Outline each uninfected red blood cell.
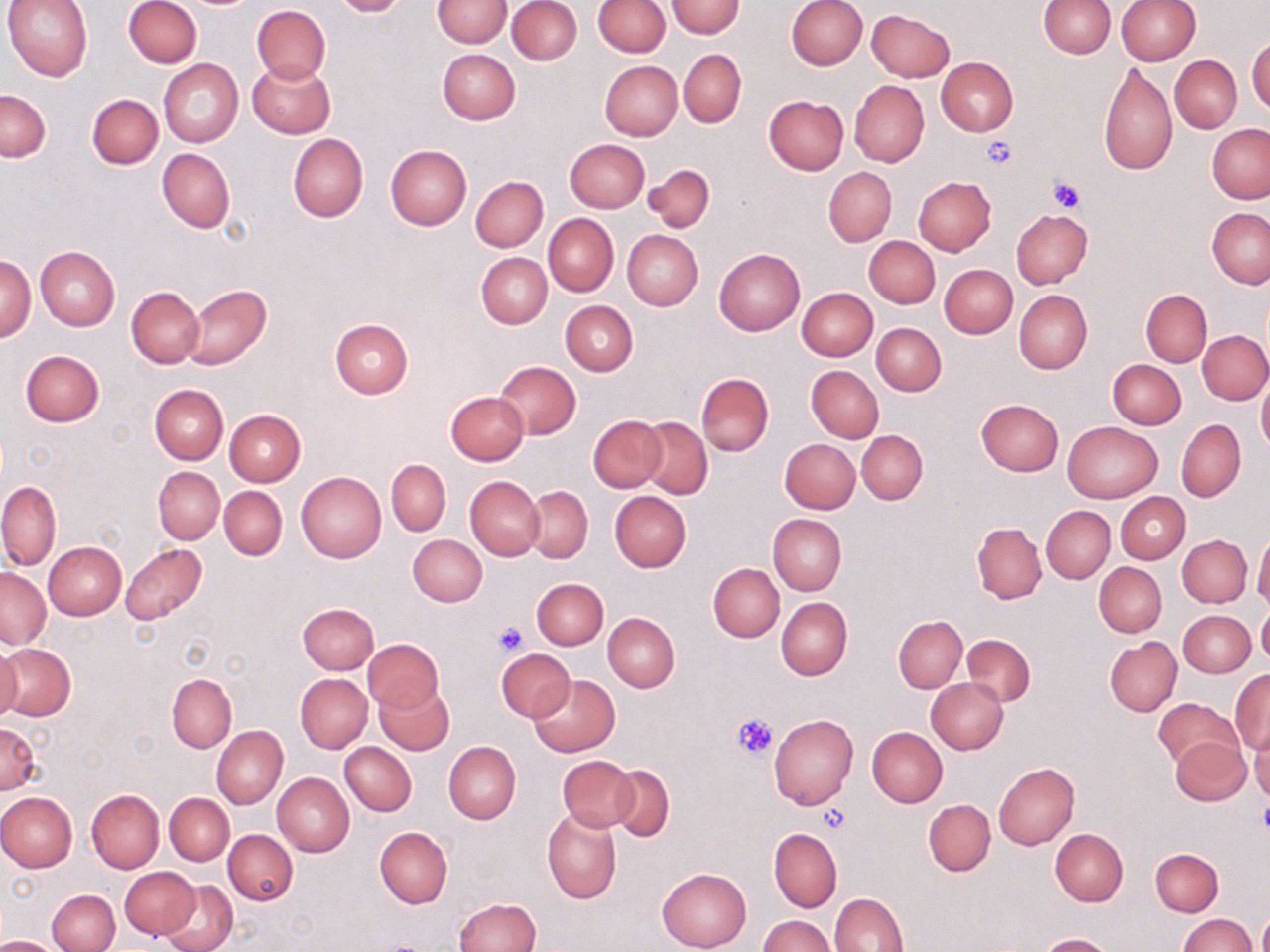
Approximate bounding boxes as [x1, y1, x2, y2] in pixels.
Uninfected red blood cells: [3, 0, 94, 81], [124, 0, 202, 68], [330, 0, 409, 17], [432, 0, 511, 48], [667, 0, 744, 37], [787, 0, 867, 70], [1038, 0, 1114, 58], [1117, 0, 1200, 65], [507, 1, 582, 64], [593, 1, 669, 56], [251, 4, 331, 84], [865, 9, 953, 81], [1247, 36, 1270, 114], [438, 49, 521, 124], [679, 50, 746, 127], [1169, 54, 1241, 133], [159, 58, 243, 147], [936, 58, 1018, 137], [599, 59, 682, 140], [246, 61, 335, 139], [1099, 62, 1177, 176], [849, 80, 929, 167], [0, 90, 50, 161], [87, 94, 163, 169], [763, 96, 848, 175], [1207, 124, 1270, 204], [288, 134, 368, 221], [565, 139, 650, 212], [385, 145, 472, 230], [157, 149, 234, 231], [643, 163, 716, 231], [824, 167, 896, 246], [470, 176, 548, 252], [913, 177, 996, 255], [1207, 208, 1270, 289], [1012, 209, 1093, 288], [544, 213, 618, 297], [622, 230, 703, 311], [864, 236, 939, 309], [35, 246, 119, 330], [714, 247, 804, 336], [476, 252, 551, 328], [1, 254, 35, 343], [940, 264, 1018, 339], [184, 285, 273, 369], [126, 286, 204, 368], [797, 287, 877, 360], [1014, 290, 1092, 374], [1141, 290, 1211, 367], [561, 300, 637, 376], [329, 317, 414, 399], [871, 323, 946, 395], [1198, 331, 1270, 404], [21, 350, 104, 427], [1108, 360, 1185, 428], [494, 361, 581, 439], [807, 365, 883, 442], [697, 373, 773, 455], [1257, 374, 1270, 455], [149, 384, 227, 464], [446, 391, 529, 465], [975, 399, 1064, 476], [225, 409, 305, 485], [588, 415, 666, 492], [639, 416, 712, 499], [1176, 419, 1247, 502], [1062, 421, 1161, 502], [856, 430, 929, 504], [780, 439, 860, 513], [386, 459, 450, 535], [153, 467, 223, 542], [296, 471, 386, 563], [466, 477, 546, 560], [0, 480, 61, 571], [219, 486, 287, 560], [525, 486, 592, 563], [610, 491, 691, 572], [1116, 492, 1189, 564], [1042, 506, 1114, 584], [768, 513, 846, 595], [972, 522, 1047, 604], [1253, 533, 1270, 611], [408, 534, 486, 606], [1178, 535, 1251, 607], [42, 541, 126, 620], [120, 543, 208, 624], [709, 563, 784, 641], [1094, 563, 1167, 637], [0, 567, 50, 648], [532, 578, 608, 650], [776, 597, 852, 680], [297, 603, 378, 674], [1257, 604, 1270, 671], [1178, 610, 1255, 677], [603, 613, 679, 692], [894, 616, 966, 692], [962, 635, 1036, 706], [1105, 637, 1182, 715], [362, 639, 443, 713], [0, 643, 76, 722], [0, 644, 22, 726], [496, 649, 575, 722], [1230, 670, 1270, 753], [167, 673, 236, 753], [296, 673, 372, 752], [528, 674, 619, 757], [927, 678, 1008, 754], [374, 681, 454, 756], [1153, 697, 1241, 769], [769, 714, 858, 810], [0, 721, 42, 794], [1249, 722, 1270, 802], [212, 725, 287, 809], [867, 727, 948, 806], [1168, 736, 1251, 805], [444, 741, 520, 824], [340, 742, 417, 816], [556, 757, 637, 831], [993, 762, 1079, 850], [608, 765, 674, 841], [273, 773, 354, 857], [86, 788, 164, 874], [0, 791, 77, 873], [165, 793, 233, 865], [923, 799, 995, 876], [543, 808, 621, 904], [375, 827, 453, 908], [769, 828, 842, 911], [1050, 829, 1128, 905], [223, 830, 297, 905], [1151, 848, 1223, 915], [120, 867, 198, 938], [657, 867, 751, 951], [158, 880, 238, 952], [47, 889, 120, 951], [831, 892, 908, 952], [453, 899, 540, 952], [1179, 912, 1255, 952], [1258, 912, 1270, 952], [759, 916, 834, 952], [1040, 933, 1113, 951], [0, 934, 61, 951].

Platelet locations: [980, 137, 1017, 169], [1048, 177, 1086, 214], [491, 620, 528, 656], [733, 714, 781, 762], [1255, 802, 1270, 833], [818, 806, 850, 834]. Slide-level diagnosis: negative for blood parasites. Optical microscopy. May-Grünwald-Giemsa stain. 1000x magnification. Single field of view. Image is 1270×952 pixels. Thin blood film.